State which cell type is depicted.
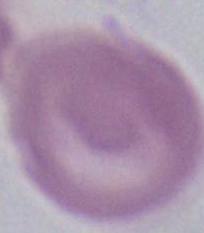

An erythrocyte.

Summary:
  - Magnification: 1000x
  - Modality: micrograph